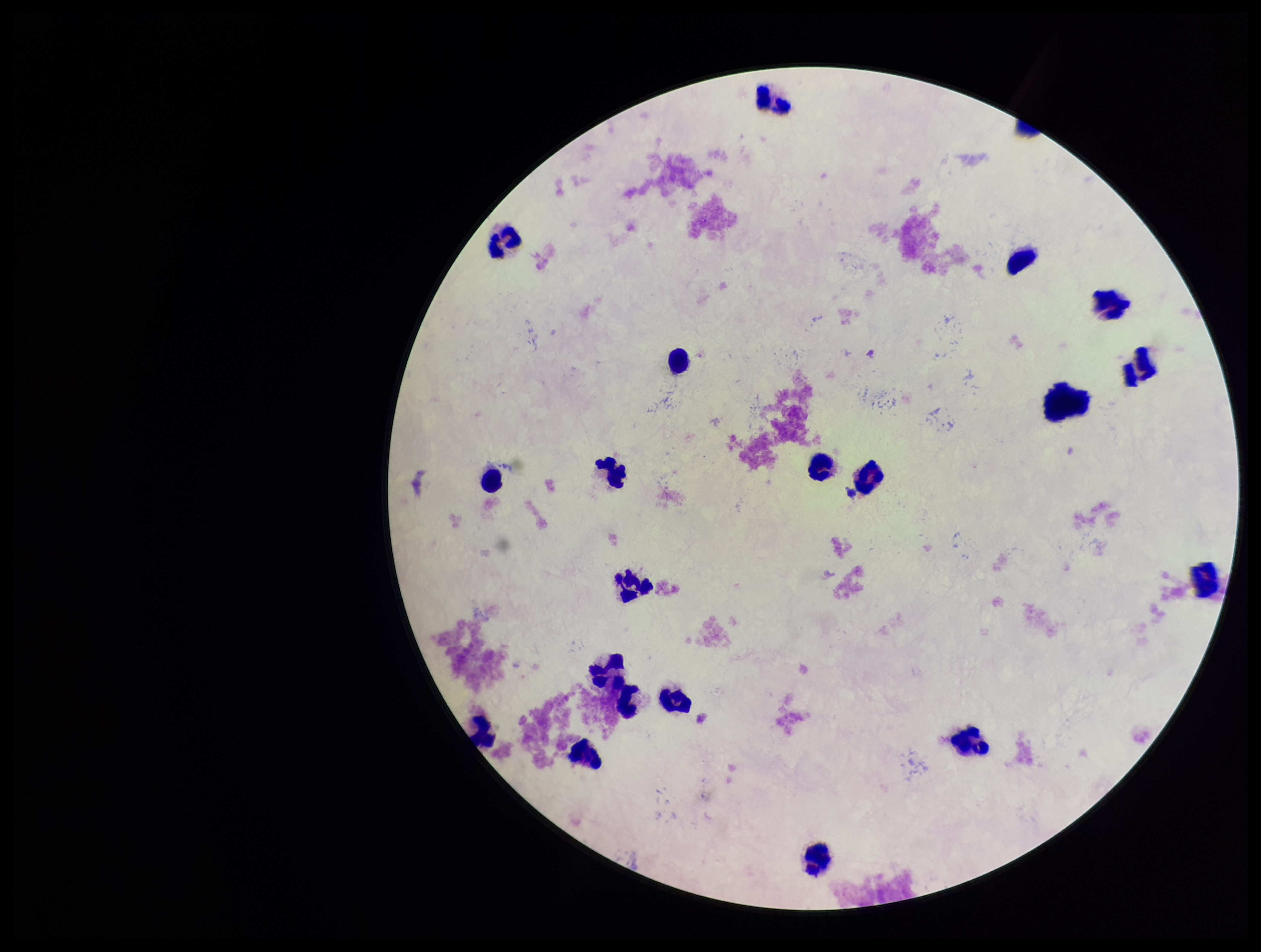
Smartphone photograph taken through the eyepiece of a microscope. Image is 1261×952 pixels. Preparation: thick smear. Parasite count: 0. Stained with Giemsa. Patient malaria status: negative. Plasmodium parasites: none seen. Single field of view. Leukocyte count: 20.